Find each parasitized red blood cell.
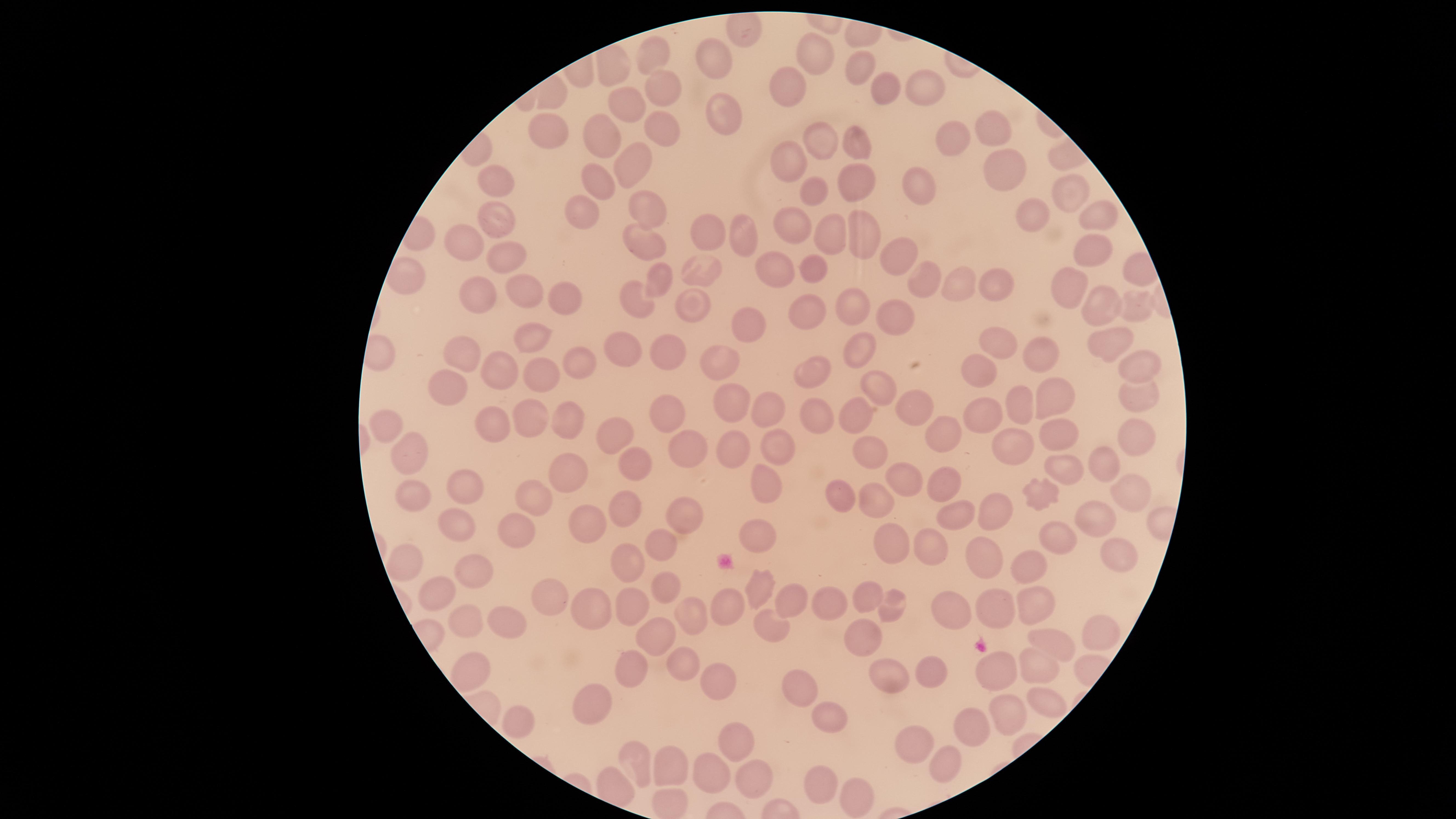

No parasitized red blood cells identified.

Approximate marker points as {x, y} in pixels.
Summary:
  - Uninfected red blood cells: {818, 47}, {653, 52}, {721, 63}, {857, 64}, {651, 84}, {920, 84}, {782, 88}, {882, 92}, {627, 106}, {725, 118}, {658, 125}, {988, 126}, {546, 133}, {600, 136}, {953, 138}, {822, 139}, {859, 148}, {630, 160}, {790, 161}, {1002, 163}, {597, 179}, {852, 181}, {499, 183}, {813, 188}, {924, 190}, {1069, 196}, {640, 205}, {583, 208}, {1103, 213}, {1030, 216}, {491, 219}, {793, 229}, {826, 232}, {711, 235}, {742, 235}, {859, 239}, {639, 240}, {462, 245}, {1084, 253}, {509, 256}, {894, 260}, {815, 265}, {775, 266}, {703, 270}, {655, 277}, {921, 281}, {992, 281}, {965, 286}, {521, 290}, {1071, 292}, {479, 293}, {559, 294}, {848, 298}, {1101, 306}, {1141, 306}, {636, 307}, {692, 308}, {808, 311}, {895, 314}, {743, 323}, {532, 335}, {1113, 342}, {857, 347}, {1002, 348}, {667, 351}, {624, 352}, {465, 356}, {1046, 356}, {577, 361}, {719, 362}, {978, 366}, {1146, 366}, {544, 372}, {810, 372}, {504, 373}, {878, 384}, {448, 389}, {1138, 398}, {726, 399}, {1052, 399}, {1022, 404}, {763, 405}, {912, 406}, {857, 408}, {980, 412}, {663, 415}, {527, 417}, {568, 417}, {813, 419}, {490, 420}, {385, 423}, {614, 434}, {1063, 434}, {1140, 434}, {951, 441}, {685, 442}, {1014, 443}, {734, 448}, {779, 448}, {869, 449}, {419, 457}, {632, 460}, {1103, 464}, {576, 470}, {1068, 471}, {899, 478}, {769, 483}, {944, 483}, {464, 485}, {1131, 487}, {534, 495}, {413, 496}, {1040, 496}, {840, 499}, {874, 499}, {621, 504}, {990, 508}, {956, 511}, {683, 515}, {1090, 515}, {456, 523}, {595, 523}, {521, 532}, {758, 533}, {1061, 541}, {662, 543}, {893, 547}, {927, 547}, {1115, 556}, {980, 559}, {405, 561}, {627, 562}, {1023, 569}, {476, 571}, {661, 582}, {761, 587}, {435, 589}, {867, 594}, {553, 598}, {632, 600}, {790, 600}, {830, 602}, {728, 605}, {894, 606}, {992, 608}, {1030, 609}, {589, 611}, {957, 611}, {687, 614}, {464, 621}, {767, 623}, {508, 627}, {858, 629}, {1099, 631}, {1054, 641}, {661, 642}, {675, 660}, {1040, 666}, {628, 667}, {471, 673}, {1002, 673}, {891, 677}, {933, 677}, {711, 679}, {799, 689}, {592, 697}, {1053, 702}, {1007, 714}, {828, 716}, {521, 722}, {967, 725}, {737, 743}, {915, 743}, {941, 764}, {636, 765}, {671, 767}, {709, 772}, {750, 778}, {818, 784}, {850, 799}
  - Image size: 1456×819 pixels
  - Visible region: circular
  - Preparation: thin blood smear
  - Field of view: single
  - Stain: Giemsa
  - Capture: smartphone photograph through the microscope eyepiece